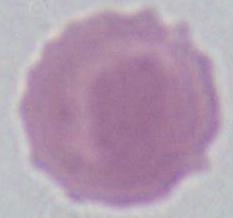

Summary:
  - Identification: red blood cell
  - Modality: micrograph
  - Magnification: 1000x